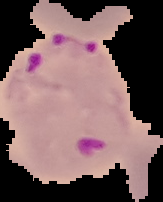

Summary:
  - Preparation: thin blood film
  - Image type: segmented cell region with the area outside set to black
  - Malaria status: parasitized
  - Image size: 163×202 pixels